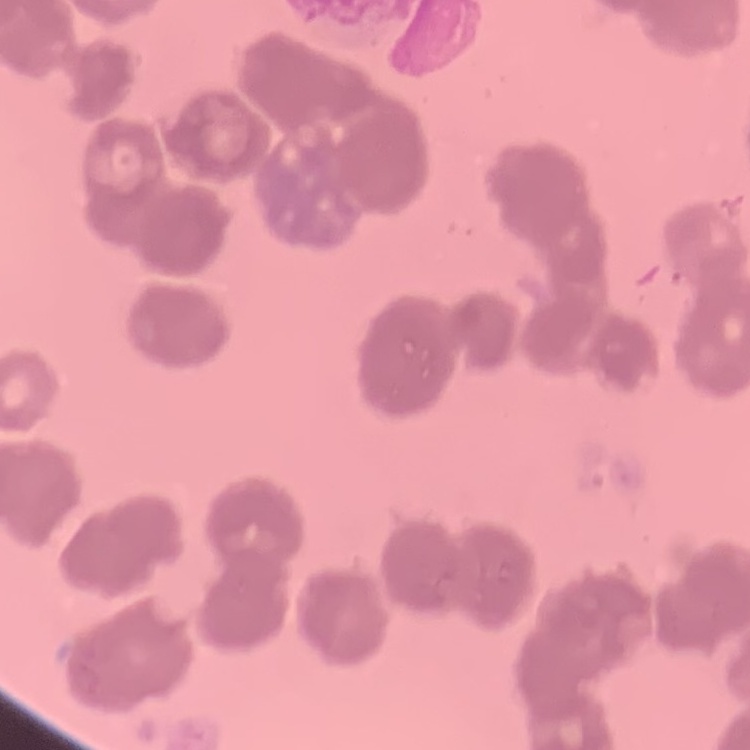

The erythrocytes exhibit rouleaux formation. Thin blood film. Stained with either Field's or Giemsa. One tile cut from a larger photomicrograph.